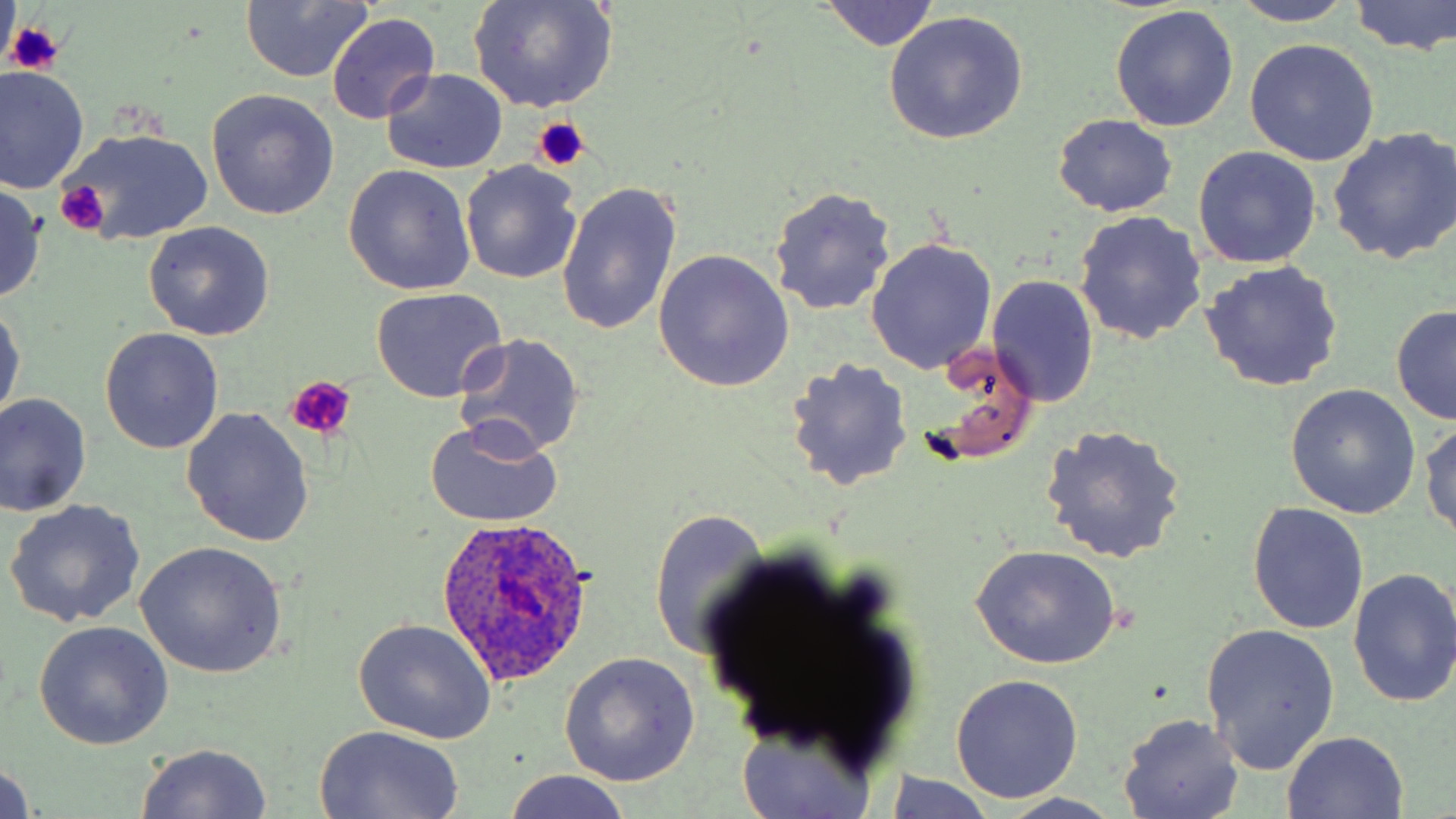 Approximate bounding boxes as [x1, y1, x2, y2] in pixels. Platelet locations: [4, 22, 65, 75], [529, 118, 592, 174], [52, 182, 110, 236], [285, 376, 356, 437]. Plasmodium ovale-infected red blood cell locations: [436, 517, 594, 684]. Uninfected red blood cell locations: [468, 0, 620, 113], [1349, 0, 1456, 57], [817, 1, 941, 51], [1228, 1, 1358, 26], [239, 2, 374, 83], [1109, 8, 1239, 132], [883, 11, 1029, 145], [327, 13, 440, 124], [1245, 39, 1379, 166], [0, 67, 88, 192], [382, 69, 508, 173], [207, 89, 339, 219], [1053, 115, 1178, 217], [59, 126, 219, 249], [1327, 128, 1456, 265], [1194, 146, 1321, 269], [460, 161, 583, 285], [342, 166, 476, 296], [555, 181, 682, 337], [0, 184, 48, 302], [769, 187, 896, 316], [1074, 211, 1208, 344], [143, 221, 275, 341], [867, 237, 997, 375], [653, 250, 795, 393], [1200, 261, 1343, 393], [988, 276, 1098, 407], [369, 287, 508, 404], [0, 296, 24, 427], [1390, 305, 1456, 425], [99, 328, 225, 454], [455, 334, 586, 458], [785, 359, 914, 491], [1286, 386, 1421, 520], [1, 393, 91, 516], [181, 407, 315, 547], [426, 417, 564, 528], [1421, 417, 1456, 546], [1040, 424, 1188, 564], [5, 501, 146, 627], [1248, 502, 1369, 635], [648, 508, 772, 659], [133, 541, 288, 679], [967, 546, 1123, 668], [1348, 567, 1456, 708], [353, 618, 498, 744], [1199, 622, 1339, 777], [34, 623, 172, 751], [559, 654, 699, 788], [949, 675, 1085, 804], [1118, 713, 1245, 819], [734, 716, 880, 819], [313, 723, 464, 818], [1282, 731, 1409, 818], [135, 743, 274, 819], [0, 759, 35, 819], [503, 770, 632, 819], [879, 772, 1001, 818], [995, 794, 1128, 819]. Slide-level diagnosis: Plasmodium ovale. May-Grünwald-Giemsa-stained preparation. Light microscopy. Captured at 1000x magnification. Image is 1456×819 pixels. One field of a larger specimen. Thin blood film.